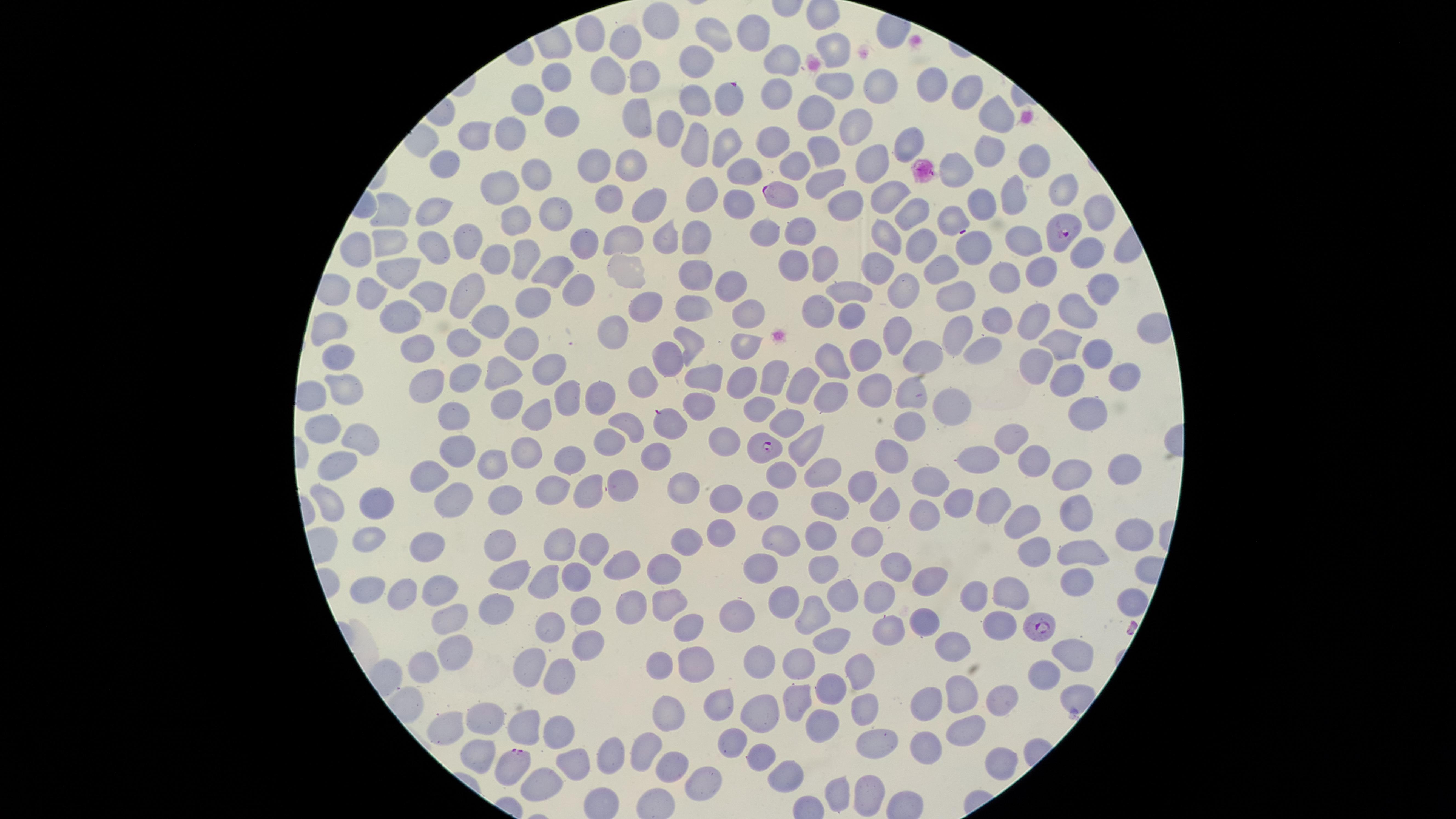

Approximate marker points as {x, y} in pixels. Uninfected RBCs: {658, 24}, {752, 33}, {588, 35}, {713, 38}, {624, 46}, {833, 51}, {780, 63}, {697, 66}, {608, 71}, {643, 78}, {559, 80}, {836, 82}, {878, 83}, {931, 87}, {962, 92}, {776, 94}, {531, 101}, {695, 102}, {821, 114}, {1000, 115}, {635, 119}, {567, 120}, {856, 120}, {669, 124}, {512, 128}, {482, 138}, {768, 141}, {908, 141}, {692, 145}, {726, 146}, {982, 147}, {830, 151}, {867, 160}, {1032, 163}, {450, 164}, {594, 164}, {955, 164}, {632, 165}, {790, 165}, {749, 169}, {535, 175}, {829, 182}, {506, 184}, {1063, 191}, {887, 192}, {709, 195}, {609, 196}, {1016, 200}, {739, 203}, {983, 204}, {846, 205}, {643, 207}, {431, 210}, {909, 211}, {551, 213}, {381, 216}, {1089, 216}, {950, 223}, {515, 225}, {802, 232}, {666, 234}, {625, 236}, {698, 237}, {880, 238}, {764, 239}, {467, 240}, {1023, 240}, {585, 244}, {384, 248}, {919, 248}, {360, 249}, {975, 249}, {1086, 251}, {435, 253}, {495, 255}, {524, 255}, {821, 259}, {792, 261}, {938, 261}, {877, 266}, {623, 267}, {1037, 269}, {547, 271}, {1007, 276}, {393, 277}, {698, 282}, {1096, 285}, {730, 287}, {902, 288}, {365, 291}, {581, 292}, {846, 292}, {952, 295}, {421, 297}, {466, 303}, {539, 303}, {641, 306}, {690, 306}, {821, 309}, {744, 310}, {1077, 313}, {401, 314}, {993, 319}, {495, 321}, {852, 323}, {333, 325}, {1029, 325}, {612, 330}, {954, 331}, {897, 337}, {463, 339}, {691, 341}, {1058, 343}, {742, 344}, {986, 345}, {413, 349}, {520, 349}, {338, 352}, {671, 355}, {863, 356}, {923, 356}, {1098, 357}, {835, 362}, {1036, 362}, {550, 363}, {503, 367}, {1126, 374}, {775, 376}, {808, 376}, {426, 377}, {462, 377}, {707, 377}, {1071, 378}, {743, 379}, {638, 380}, {345, 385}, {875, 386}, {598, 389}, {907, 391}, {832, 393}, {566, 394}, {510, 399}, {950, 402}, {702, 404}, {535, 410}, {326, 417}, {1083, 417}, {455, 419}, {670, 421}, {627, 428}, {909, 428}, {1014, 437}, {606, 439}, {722, 439}, {804, 445}, {360, 449}, {462, 452}, {656, 453}, {525, 454}, {1036, 454}, {886, 456}, {983, 458}, {571, 460}, {1124, 464}, {490, 467}, {825, 468}, {1074, 469}, {337, 472}, {777, 474}, {430, 476}, {622, 476}, {927, 478}, {860, 480}, {590, 487}, {558, 488}, {686, 488}, {727, 497}, {451, 500}, {379, 502}, {499, 502}, {959, 503}, {327, 505}, {762, 505}, {828, 505}, {885, 505}, {989, 509}, {1079, 516}, {920, 517}, {1013, 523}, {720, 535}, {819, 536}, {1123, 537}, {865, 538}, {782, 539}, {368, 540}, {687, 541}, {592, 545}, {1039, 545}, {558, 546}, {498, 547}, {1084, 548}, {432, 551}, {620, 565}, {760, 566}, {898, 567}, {820, 569}, {547, 570}, {659, 571}, {512, 573}, {1076, 576}, {573, 579}, {932, 582}, {442, 583}, {371, 586}, {973, 587}, {1018, 590}, {405, 591}, {842, 595}, {880, 595}, {665, 597}, {780, 597}, {1124, 601}, {494, 610}, {810, 610}, {636, 611}, {739, 611}, {588, 612}, {930, 619}, {452, 621}, {997, 623}, {549, 626}, {689, 628}, {883, 628}, {836, 640}, {585, 641}, {955, 643}, {1072, 652}, {453, 653}, {760, 659}, {695, 662}, {416, 664}, {662, 666}, {526, 668}, {799, 668}, {860, 669}, {1039, 675}, {558, 678}, {832, 689}, {793, 696}, {924, 696}, {962, 696}, {1001, 699}, {717, 702}, {862, 705}, {668, 712}, {760, 715}, {525, 717}, {488, 718}, {821, 719}, {452, 723}, {964, 730}, {559, 734}, {738, 735}, {866, 742}, {920, 747}, {645, 748}, {764, 751}, {472, 757}, {994, 757}, {613, 758}, {582, 763}, {671, 765}, {788, 773}, {700, 778}, {542, 781}, {838, 788}, {864, 792}. Parasitized RBCs: {727, 97}, {779, 195}, {1058, 232}, {766, 447}, {1040, 627}, {516, 762}. Species: Plasmodium falciparum. Photographed with a smartphone camera through the microscope eyepiece. Thin smear of blood. Single field of view. Circular visible region. Giemsa stain. Presence: malaria parasites seen. Image is 1456×819 pixels.